Report the malaria status of this cell.
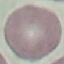
It is uninfected.

stain = Giemsa
image type = cell patch, automatically extracted from a larger field of view and resized to 64 × 64 pixels
preparation = thin blood smear
capture = smartphone camera at the microscope eyepiece